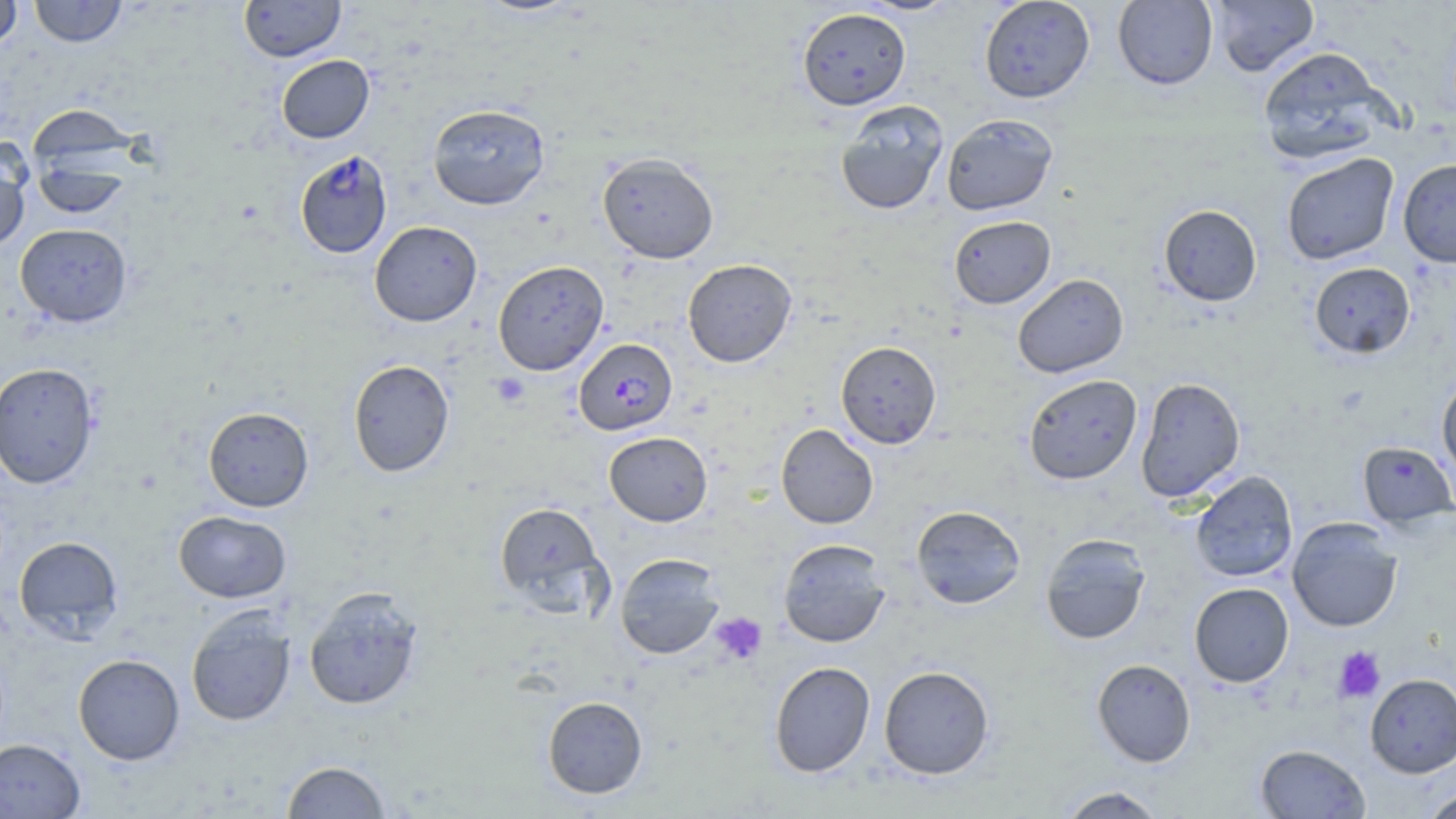
{
  "slide_level_diagnosis": "Plasmodium falciparum",
  "magnification": "1000x",
  "preparation": "thin blood film",
  "platelet_locations": "approximate bounding boxes as (x1,y1)-(x2,y2) corner pairs in pixels: (491,373)-(530,407), (710,612)-(767,665), (1333,646)-(1385,703)",
  "uninfected_red_blood_cell_locations": "approximate bounding boxes as (x1,y1)-(x2,y2) corner pairs in pixels: (0,0)-(22,51), (29,0)-(127,47), (855,0)-(960,16), (979,0)-(1095,103), (1113,0)-(1218,89), (1207,0)-(1320,77), (239,1)-(345,62), (797,7)-(911,110), (1257,46)-(1393,164), (276,55)-(374,143), (835,100)-(950,215), (427,104)-(550,209), (941,113)-(1058,215), (26,116)-(140,216), (0,140)-(31,252), (598,152)-(719,264), (1281,153)-(1399,265), (1397,159)-(1456,267), (1158,204)-(1262,306), (948,215)-(1056,308), (369,221)-(482,326), (15,223)-(132,327), (682,259)-(797,367), (492,260)-(609,376), (1309,262)-(1416,358), (1013,274)-(1128,378), (836,340)-(942,449), (348,359)-(454,477), (0,362)-(100,489), (1023,374)-(1142,485), (1437,375)-(1456,480), (1135,377)-(1246,503), (203,406)-(314,512), (776,424)-(878,529), (604,431)-(713,526), (1357,440)-(1456,529), (1189,470)-(1298,582), (494,501)-(607,614), (911,505)-(1026,609), (174,510)-(291,603), (1287,517)-(1403,632), (1040,533)-(1151,644), (14,536)-(124,640), (778,538)-(891,647), (615,553)-(725,659), (1189,582)-(1294,687), (303,586)-(424,710), (186,607)-(296,726), (73,654)-(185,765), (1092,659)-(1196,767), (769,661)-(875,778), (879,665)-(994,779), (1366,673)-(1456,777), (542,696)-(648,798), (0,738)-(86,818), (1255,743)-(1371,818), (281,760)-(392,818), (1057,786)-(1166,818), (1421,787)-(1456,819)",
  "plasmodium_falciparum_infected_red_blood_cell_locations": "approximate bounding boxes as (x1,y1)-(x2,y2) corner pairs in pixels: (294,150)-(393,258), (574,338)-(677,435)",
  "stain": "May-Grünwald-Giemsa",
  "modality": "optical microscopy",
  "field_of_view": "one of a larger specimen",
  "image_size": "1456×819 pixels"
}